Identify the parasite.
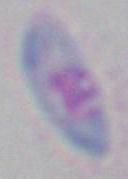
This is Toxoplasma gondii.

Photomicrograph. 1000x magnification.